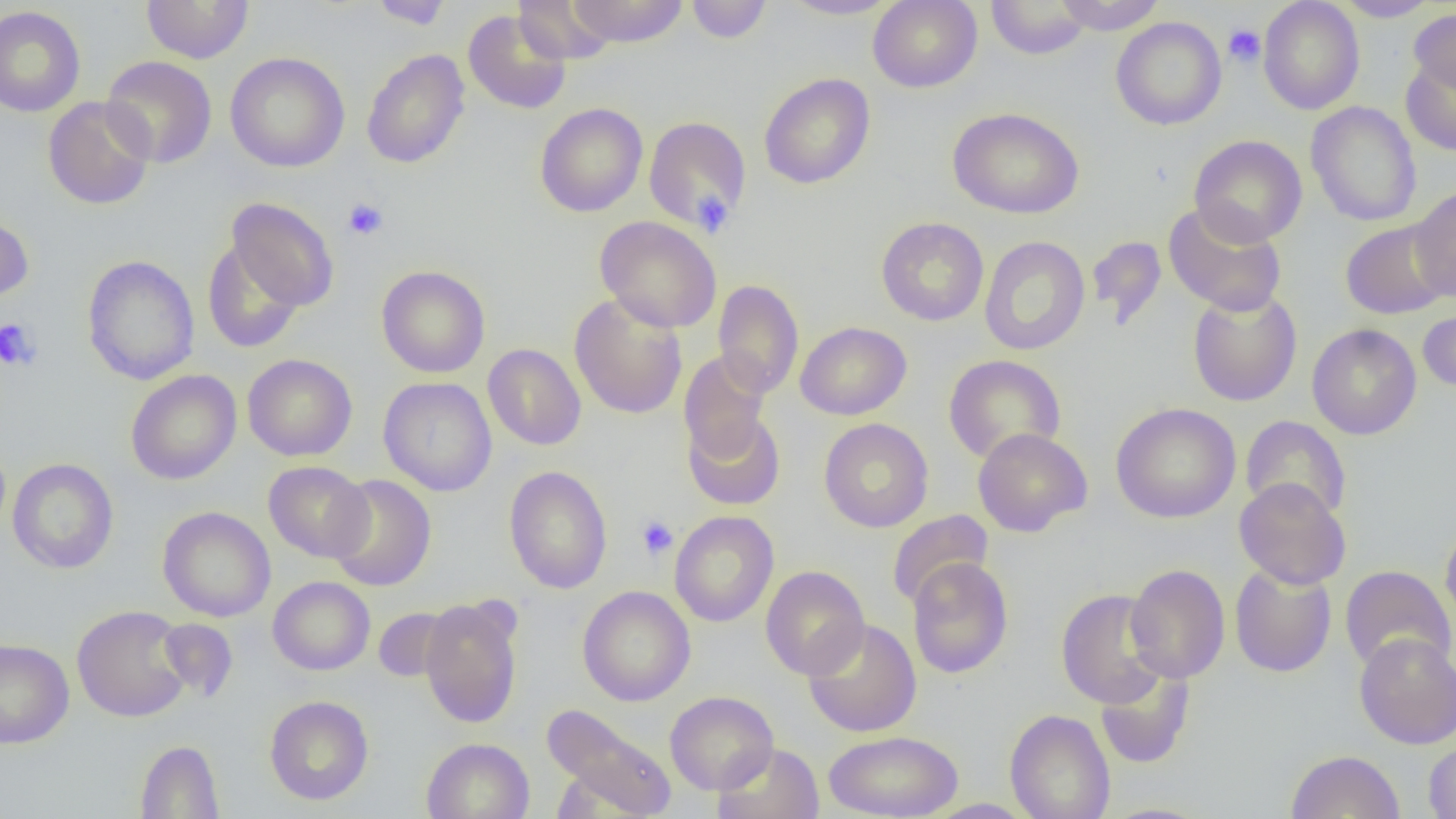
slide_level_diagnosis: no evidence of blood parasites
uninfected_red_blood_cell_locations: 'approximate bounding boxes as (x1,y1)-(x2,y2) corner pairs in pixels: (141,0)-(255,64), (369,0)-(454,29), (512,0)-(617,65), (568,0)-(689,47), (686,0)-(772,43), (780,0)-(901,20), (868,0)-(982,92), (1053,0)-(1166,35), (1258,0)-(1364,115), (1334,0)-(1440,21), (985,1)-(1093,59), (0,6)-(85,117), (1409,7)-(1456,97), (462,9)-(571,115), (1111,16)-(1227,130), (361,49)-(469,169), (224,52)-(350,172), (102,55)-(217,168), (1401,57)-(1456,156), (758,72)-(875,189), (43,96)-(155,210), (1306,101)-(1422,227), (534,102)-(648,217), (947,107)-(1084,219), (643,116)-(752,232), (1189,135)-(1307,246), (1410,186)-(1456,301), (227,198)-(339,312), (1162,202)-(1288,317), (0,211)-(34,303), (594,215)-(722,333), (876,217)-(989,326), (1340,219)-(1453,319), (979,236)-(1090,356), (1087,237)-(1167,329), (202,239)-(306,354), (81,254)-(200,385), (376,265)-(490,378), (712,279)-(804,399), (1188,287)-(1302,407), (569,293)-(688,419), (1418,307)-(1456,394), (795,321)-(911,420), (1306,323)-(1422,440), (483,343)-(586,450), (679,350)-(772,465), (243,353)-(357,460), (943,354)-(1066,464), (126,369)-(241,485), (378,376)-(497,496), (1111,402)-(1240,523), (683,412)-(786,511), (1240,415)-(1352,522), (819,418)-(934,532), (973,427)-(1092,537), (7,458)-(118,574), (263,461)-(374,562), (504,465)-(612,594), (326,474)-(437,591), (1234,477)-(1351,590), (157,506)-(276,622), (886,509)-(994,610), (670,510)-(779,627), (1440,523)-(1456,629), (907,557)-(1013,678), (1229,562)-(1337,678), (1125,564)-(1230,683), (760,565)-(870,680), (1340,565)-(1456,675), (268,576)-(375,675), (578,586)-(695,706), (1056,588)-(1171,709), (420,596)-(523,728), (71,605)-(192,722), (373,607)-(455,682), (803,617)-(922,738), (156,619)-(239,701), (1354,632)-(1456,749), (0,638)-(74,749), (1095,664)-(1196,770), (664,691)-(778,794), (265,695)-(374,805), (542,703)-(677,817), (1005,709)-(1116,819), (823,730)-(963,818), (421,737)-(534,819), (1423,737)-(1456,819), (134,740)-(224,818), (713,742)-(824,819), (1286,750)-(1405,819), (922,798)-(1034,818), (1096,802)-(1217,819)'
preparation: thin blood smear
magnification: 1000x
field_of_view: single
image_size: 1456×819 pixels
modality: light microscopy
platelet_locations: 'approximate bounding boxes as (x1,y1)-(x2,y2) corner pairs in pixels: (1223,24)-(1266,67), (692,190)-(733,236), (342,198)-(388,240), (0,318)-(41,372), (636,515)-(678,560)'